Outline each blood parasite and name the species.
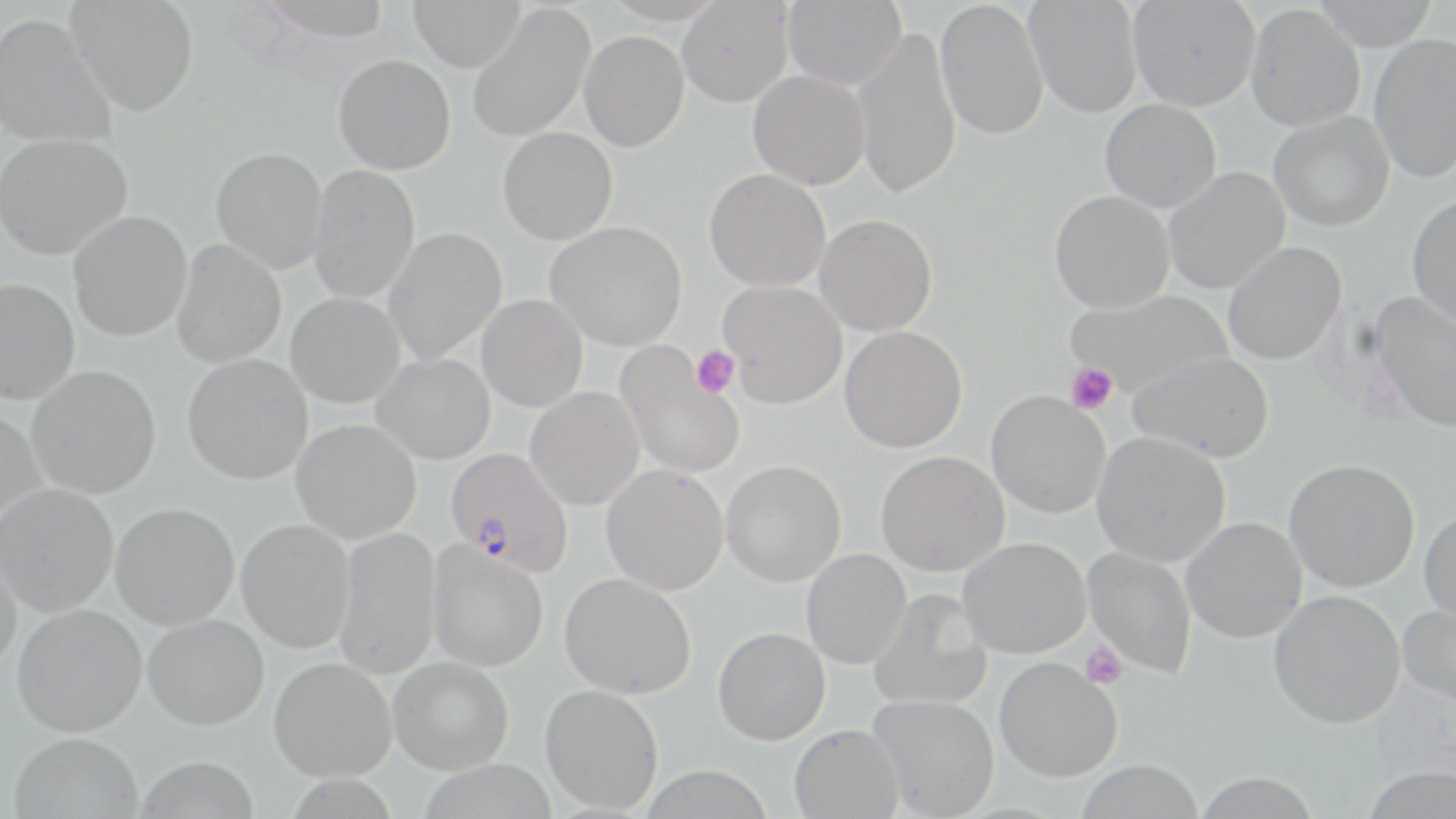
Approximate bounding boxes as [x1, y1, x2, y2] in pixels.
Plasmodium falciparum-infected red blood cells: [445, 447, 574, 576].
No Plasmodium ovale, Plasmodium malariae, Plasmodium vivax, Babesia divergens, or Trypanosoma brucei observed.

slide-level diagnosis = Plasmodium falciparum
field of view = one of a larger specimen
preparation = thin blood film
uninfected red blood cell locations = approximate bounding boxes as [x1, y1, x2, y2] in pixels: [67, 0, 199, 116], [408, 0, 525, 71], [782, 0, 906, 90], [935, 0, 1049, 141], [1024, 0, 1142, 118], [1128, 0, 1260, 110], [1311, 0, 1440, 50], [677, 1, 793, 107], [468, 4, 595, 142], [1245, 5, 1365, 131], [0, 12, 117, 149], [851, 28, 963, 198], [580, 30, 689, 151], [1369, 34, 1456, 184], [334, 54, 455, 174], [748, 70, 870, 189], [1100, 99, 1221, 212], [1269, 110, 1394, 231], [498, 127, 617, 244], [0, 133, 133, 260], [211, 147, 327, 274], [308, 164, 420, 304], [1163, 167, 1290, 295], [704, 169, 831, 293], [1049, 190, 1174, 313], [1407, 194, 1456, 326], [68, 211, 192, 341], [815, 214, 937, 336], [546, 221, 687, 351], [382, 227, 506, 364], [172, 239, 286, 368], [1222, 241, 1346, 365], [0, 279, 80, 406], [718, 279, 848, 407], [1064, 289, 1235, 399], [1370, 291, 1456, 432], [285, 292, 405, 408], [477, 294, 587, 412], [840, 326, 967, 453], [616, 344, 745, 478], [1128, 351, 1274, 462], [371, 353, 495, 464], [183, 354, 313, 484], [26, 365, 161, 498], [525, 386, 644, 511], [986, 390, 1110, 518], [0, 408, 46, 531], [291, 419, 421, 544], [1092, 431, 1230, 567], [875, 450, 1009, 576], [1284, 458, 1420, 593], [721, 460, 846, 586], [601, 464, 729, 596], [0, 483, 119, 617], [110, 503, 239, 630], [1419, 508, 1456, 624], [1181, 517, 1307, 643], [237, 519, 354, 653], [334, 527, 441, 679], [958, 537, 1091, 658], [427, 542, 548, 672], [0, 543, 23, 675], [1082, 547, 1197, 679], [801, 549, 910, 669], [560, 572, 696, 699], [868, 589, 992, 711], [1268, 589, 1405, 728], [1398, 603, 1456, 708], [12, 604, 146, 737], [143, 614, 269, 730], [713, 627, 830, 745], [269, 657, 396, 781], [388, 657, 513, 774], [995, 657, 1122, 782], [540, 684, 664, 813], [868, 694, 999, 817], [789, 723, 903, 818], [8, 732, 143, 819], [135, 754, 259, 818], [1075, 759, 1203, 819]
modality = optical microscopy
platelet locations = approximate bounding boxes as [x1, y1, x2, y2] in pixels: [691, 345, 741, 398], [1065, 362, 1118, 415], [1080, 643, 1128, 689]
image size = 1456×819 pixels
stain = May-Grünwald-Giemsa
magnification = 1000x